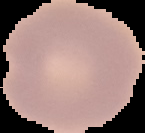

result: negative for malaria parasites
image_type: segmented cell region on a black background
preparation: thin blood film
image_size: 145×133 pixels